Locate every uninfected red blood cell.
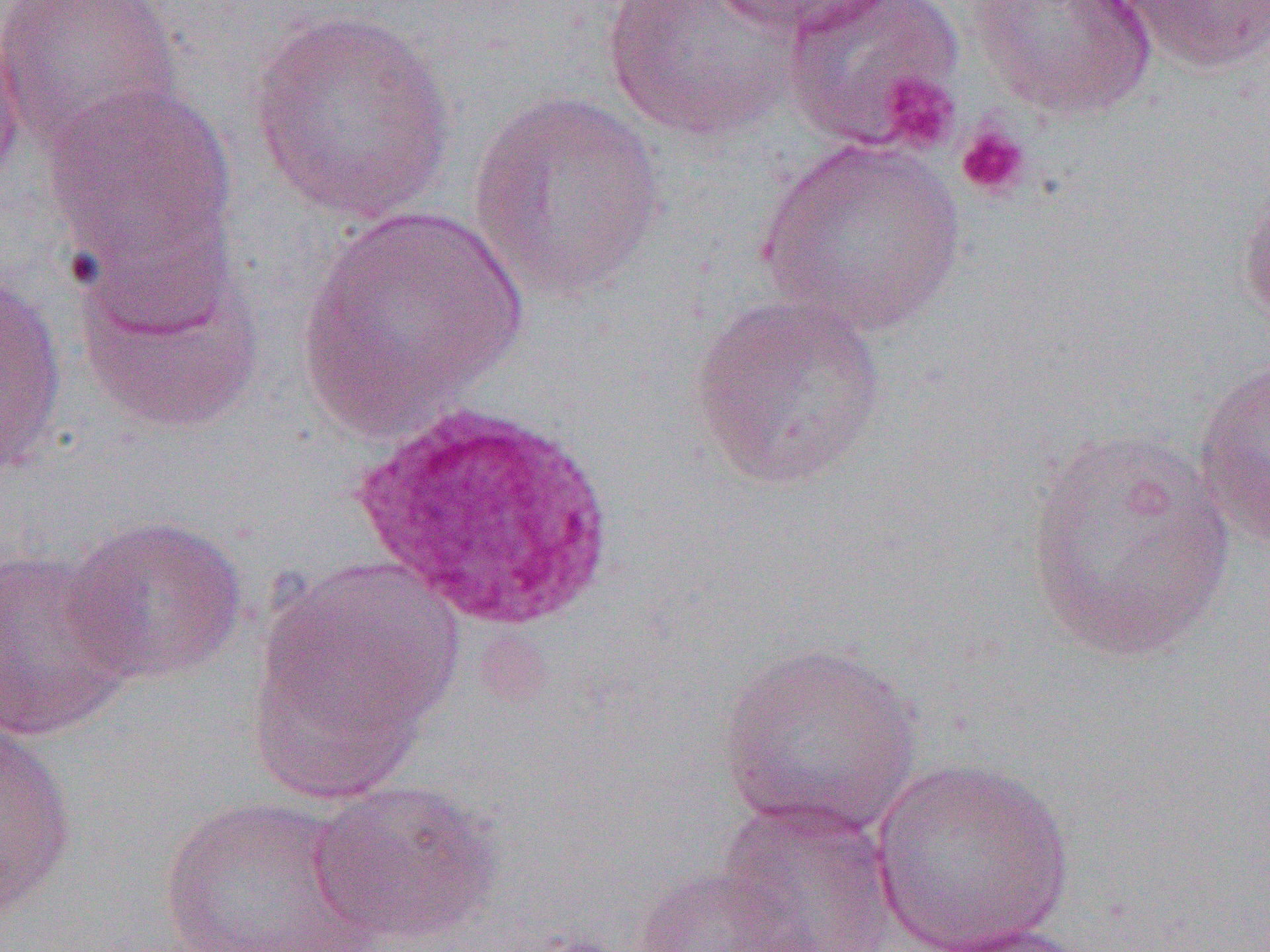

Approximate bounding boxes as (x1,y1)-(x2,y2) corner pairs in pixels.
Uninfected red blood cells: (1,0)-(183,156), (599,0)-(803,142), (703,0)-(888,37), (783,0)-(966,151), (966,0)-(1159,122), (1107,1)-(1270,75), (247,8)-(462,224), (0,21)-(28,194), (41,81)-(238,285), (466,89)-(669,305), (756,137)-(968,336), (1237,185)-(1270,337), (299,202)-(530,439), (72,233)-(269,437), (0,268)-(69,478), (688,294)-(888,491), (1191,356)-(1270,549), (1022,427)-(1235,662), (62,513)-(249,686), (0,548)-(139,741), (249,561)-(460,782), (716,640)-(924,838), (0,722)-(79,920), (868,758)-(1076,952), (308,778)-(500,947), (158,795)-(378,952), (713,795)-(902,952), (630,865)-(808,952), (922,921)-(1093,952).

Platelet locations: (878,72)-(960,154), (955,122)-(1033,201). Slide-level diagnosis: Plasmodium ovale. Thin blood smear. Single field of view. Image is 1270×952 pixels. 1000x magnification. Light microscopy.